State the blood parasite species.
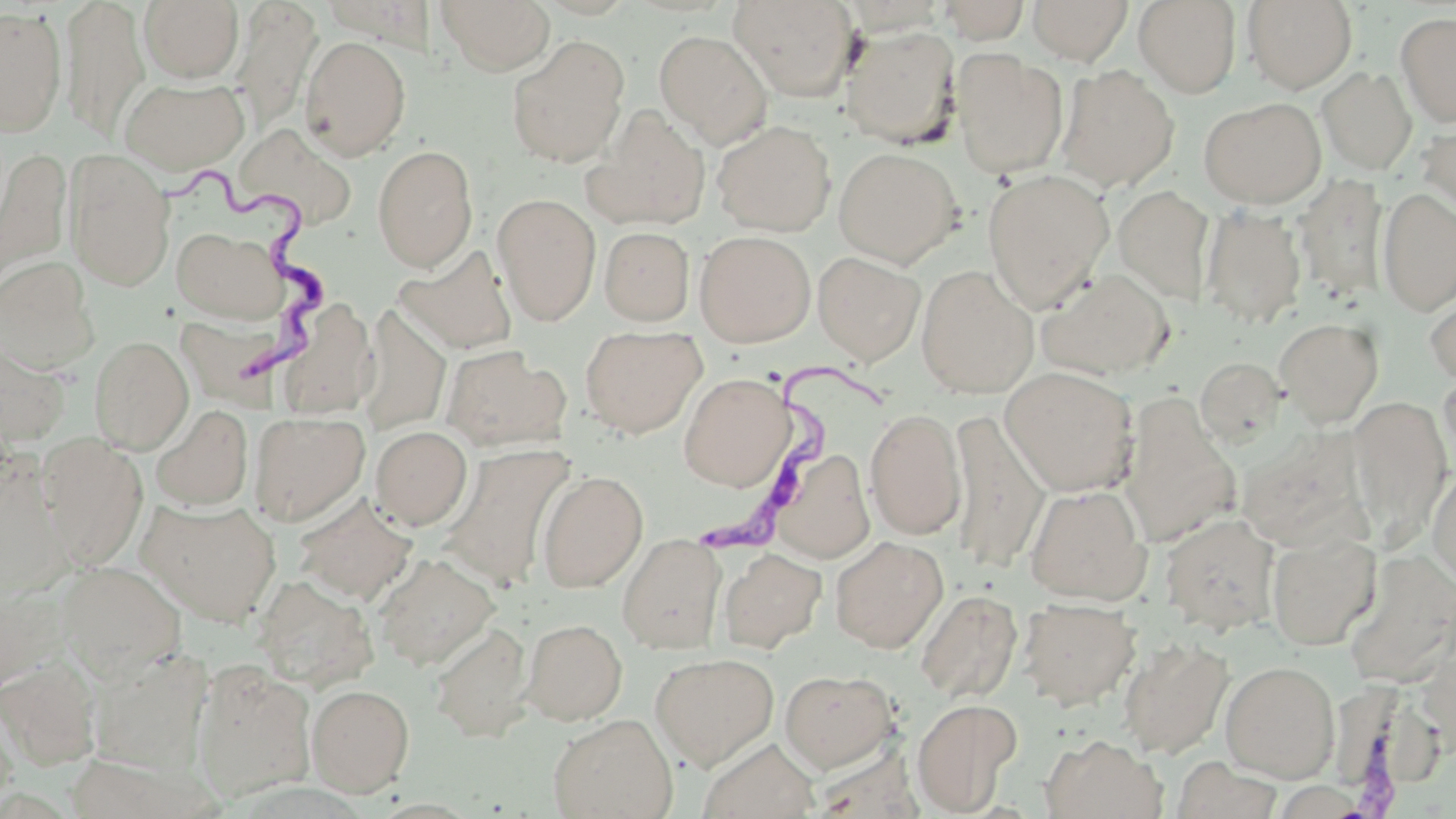
Trypanosoma brucei.

Approximate bounding boxes as (x1,y1)-(x2,y2) corner pairs in pixels. Trypanosoma brucei locations: (154,168)-(342,396), (684,356)-(906,556). Uninfected red blood cell locations: (59,0)-(149,140), (139,0)-(244,83), (436,0)-(555,75), (728,0)-(857,101), (938,0)-(1030,44), (1028,0)-(1133,65), (1133,0)-(1241,97), (1241,0)-(1358,93), (231,2)-(321,135), (0,5)-(66,137), (1395,11)-(1456,128), (840,24)-(961,148), (654,30)-(773,148), (299,35)-(411,160), (507,37)-(630,168), (952,51)-(1069,178), (1056,65)-(1180,193), (1317,66)-(1417,175), (119,76)-(250,174), (1198,97)-(1327,209), (585,106)-(712,231), (1417,118)-(1456,227), (712,120)-(836,236), (234,123)-(357,229), (372,144)-(478,272), (0,146)-(72,293), (833,147)-(963,267), (63,149)-(175,291), (982,169)-(1114,311), (1293,174)-(1389,302), (1113,184)-(1216,305), (1376,187)-(1456,316), (493,193)-(601,326), (1200,205)-(1307,329), (171,226)-(287,324), (599,226)-(695,325), (694,230)-(816,347), (394,245)-(519,356), (813,251)-(926,366), (0,257)-(99,373), (916,264)-(1038,399), (1037,268)-(1176,380), (1423,281)-(1456,388), (277,298)-(380,420), (357,305)-(451,437), (1274,318)-(1384,427), (580,325)-(706,438), (89,336)-(194,453), (0,339)-(71,449), (441,345)-(570,452), (1195,356)-(1287,449), (1438,365)-(1456,476), (1000,366)-(1140,496), (679,372)-(794,491), (1118,396)-(1240,549), (1348,396)-(1453,544), (151,404)-(253,511), (864,408)-(967,540), (947,409)-(1050,573), (249,411)-(370,526), (370,426)-(472,529), (37,436)-(148,569), (440,444)-(574,589), (773,451)-(875,563), (1,457)-(72,601), (1426,463)-(1456,590), (537,470)-(648,592), (1024,484)-(1151,604), (294,494)-(417,605), (139,498)-(282,627), (1160,513)-(1281,635), (1266,530)-(1382,650), (617,533)-(727,653), (830,535)-(948,653), (718,547)-(826,652), (1343,548)-(1456,687), (373,552)-(499,669), (55,560)-(186,680), (251,574)-(378,691), (0,582)-(67,692), (915,590)-(1022,704), (1018,598)-(1141,709), (522,618)-(627,725), (430,621)-(534,742), (1119,637)-(1233,759), (86,648)-(213,775), (650,652)-(779,771), (0,656)-(101,771), (191,661)-(317,804), (1220,661)-(1339,782), (779,668)-(899,773), (307,683)-(414,796), (911,698)-(1023,815), (0,706)-(17,816), (548,713)-(678,819), (1041,734)-(1166,819), (698,736)-(820,819). Light microscopy. May-Grünwald-Giemsa stain. 1000x magnification. One field of a larger specimen. Image is 1456×819 pixels. Thin blood smear.